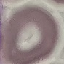

malaria_status: uninfected
capture: smartphone through the microscope eyepiece
stain: Giemsa
image_type: automatically extracted cell patch, resized to 64 × 64 pixels
preparation: thin blood film